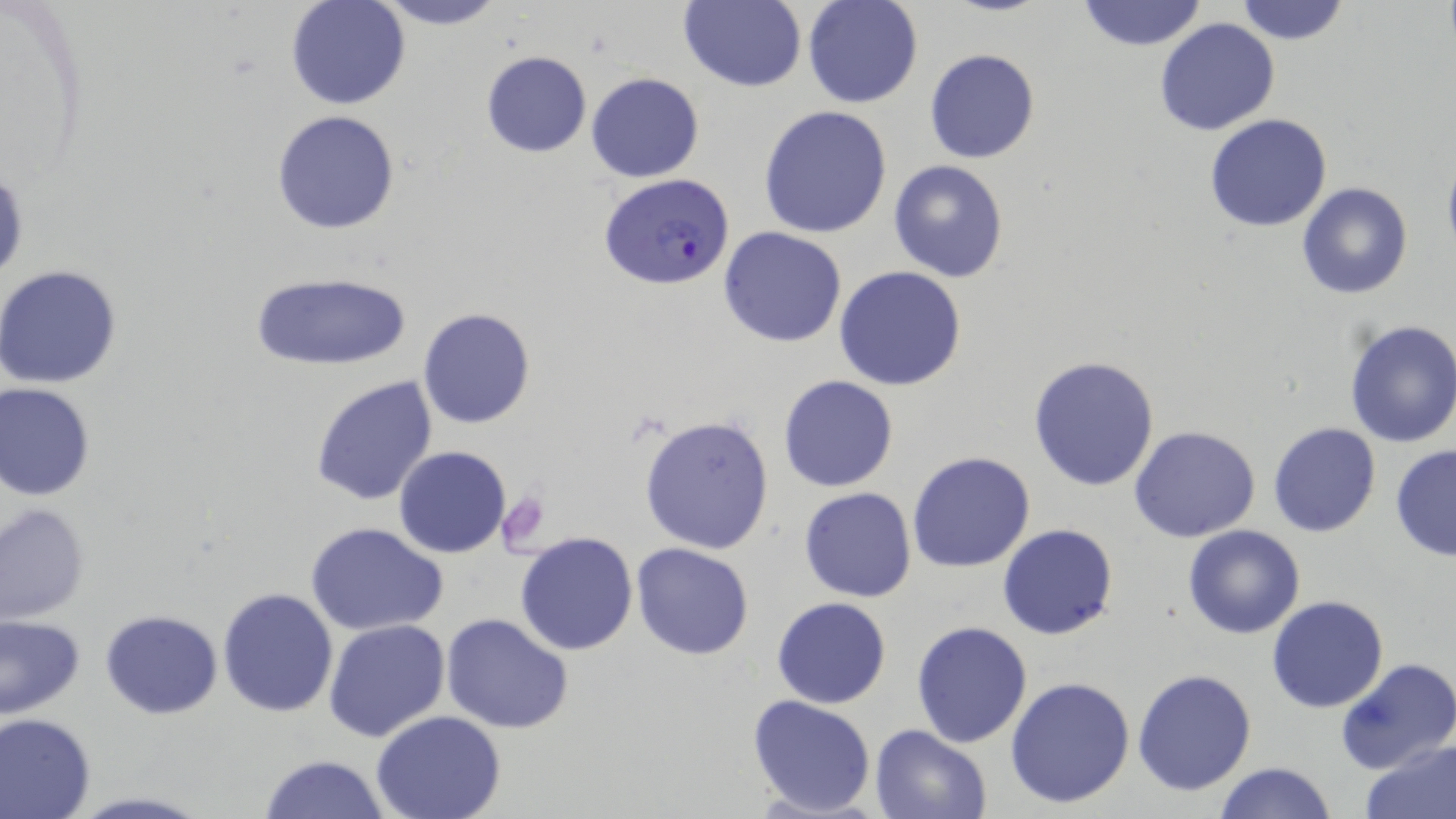

Summary:
  - Coordinate format: approximate bounding boxes as (x1,y1)-(x2,y2) corner pairs in pixels
  - Plasmodium falciparum-infected red blood cell locations: (599,173)-(736,293)
  - Uninfected red blood cell locations: (368,0)-(510,30), (677,0)-(807,92), (801,0)-(923,109), (1075,0)-(1208,52), (1233,0)-(1350,45), (286,1)-(410,110), (1154,18)-(1280,136), (924,48)-(1040,164), (481,50)-(592,157), (586,72)-(703,183), (758,105)-(892,238), (270,111)-(401,233), (1203,114)-(1333,232), (1441,153)-(1456,261), (888,159)-(1010,282), (1296,183)-(1412,299), (719,227)-(848,347), (0,265)-(122,389), (834,265)-(967,391), (250,271)-(412,371), (418,307)-(536,429), (1342,317)-(1456,448), (1028,354)-(1161,491), (310,375)-(439,506), (777,375)-(899,492), (1,383)-(97,500), (638,414)-(774,554), (1267,422)-(1382,537), (1128,426)-(1261,543), (395,445)-(511,558), (1390,445)-(1456,562), (906,451)-(1037,573), (798,487)-(918,603), (1,503)-(90,624), (307,523)-(446,637), (998,524)-(1118,641), (1182,524)-(1305,639), (514,532)-(638,656), (631,542)-(755,660), (217,587)-(340,718), (772,596)-(891,709), (1266,596)-(1389,713), (100,609)-(222,718), (440,613)-(574,733), (0,614)-(85,721), (324,619)-(449,741), (912,621)-(1034,748), (1335,657)-(1456,775), (1132,668)-(1256,795), (1005,675)-(1136,810), (748,694)-(877,818), (370,711)-(509,819), (0,712)-(97,819), (869,724)-(990,819), (1360,738)-(1456,819), (257,754)-(392,819), (1213,763)-(1337,818), (60,792)-(216,819)
  - Platelet locations: (499,490)-(551,553)
  - Slide-level diagnosis: Plasmodium falciparum
  - Magnification: 1000x
  - Image size: 1456×819 pixels
  - Modality: optical microscopy
  - Field of view: one of a larger specimen
  - Stain: May-Grünwald-Giemsa
  - Preparation: thin blood smear